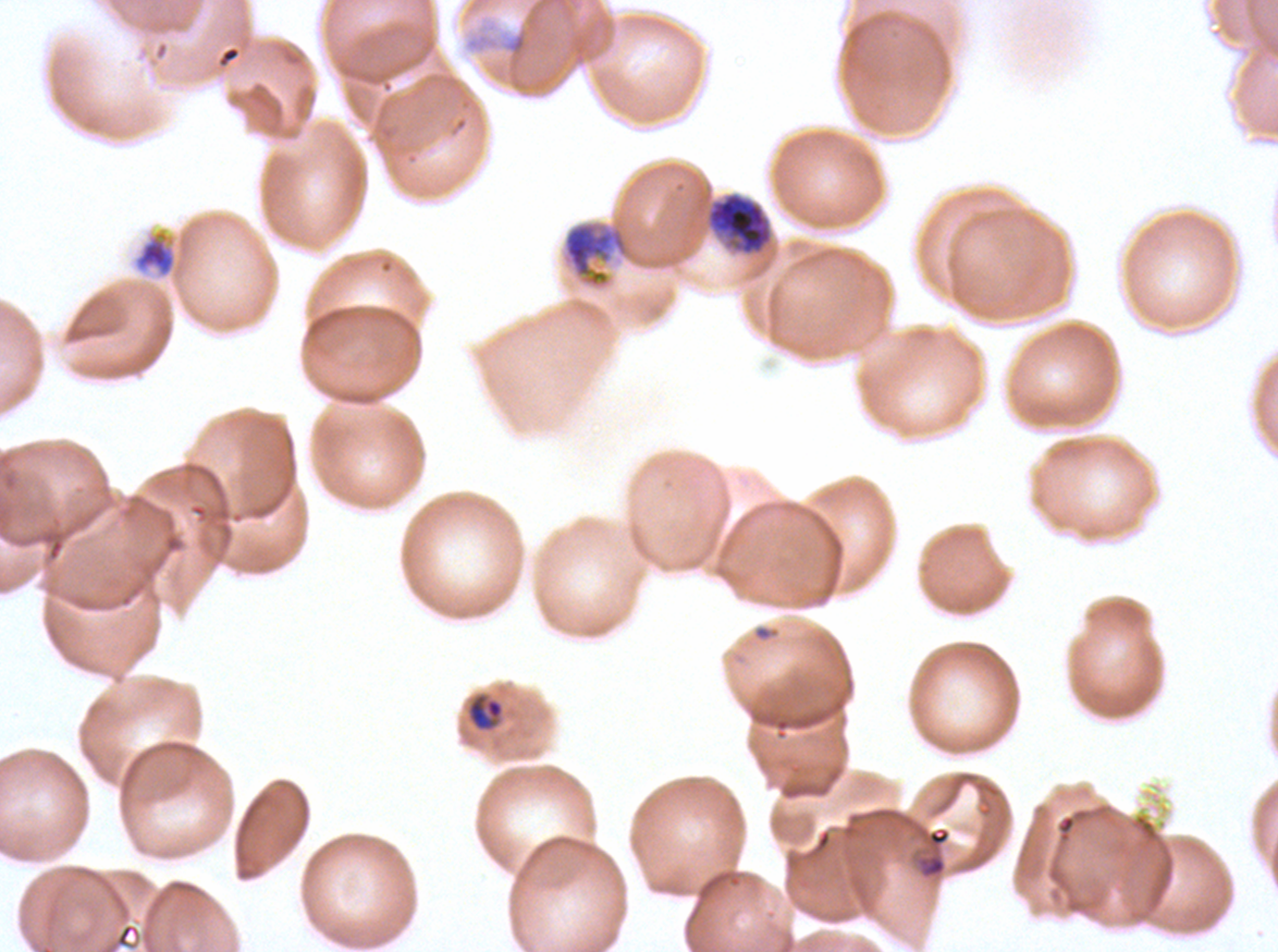
late_trophozoite_locations: 'approximate bounding boxes as [x1, y1, x2, y2] in pixels: [563, 222, 626, 287]'
image_size: 1278×952 pixels
mid_trophozoite_locations: 'approximate bounding boxes as [x1, y1, x2, y2] in pixels: [132, 228, 178, 279]'
field_of_view: one sub-image of a larger composite
life_cycle_stages_observed: late-ring/early-trophozoite, mid trophozoite, late trophozoite, early schizont
specimen: P. falciparum from a patient in The Gambia, cultured ex vivo for 24 to 48 hours
debris_locations: 'approximate bounding boxes as [x1, y1, x2, y2] in pixels: [506, 31, 527, 55]'
preparation: thin blood film
early_schizont_locations: 'approximate bounding boxes as [x1, y1, x2, y2] in pixels: [706, 191, 773, 256]'
late_ring_early_trophozoite_locations: 'approximate bounding boxes as [x1, y1, x2, y2] in pixels: [468, 698, 503, 729], [914, 825, 952, 880]'
stain: Giemsa